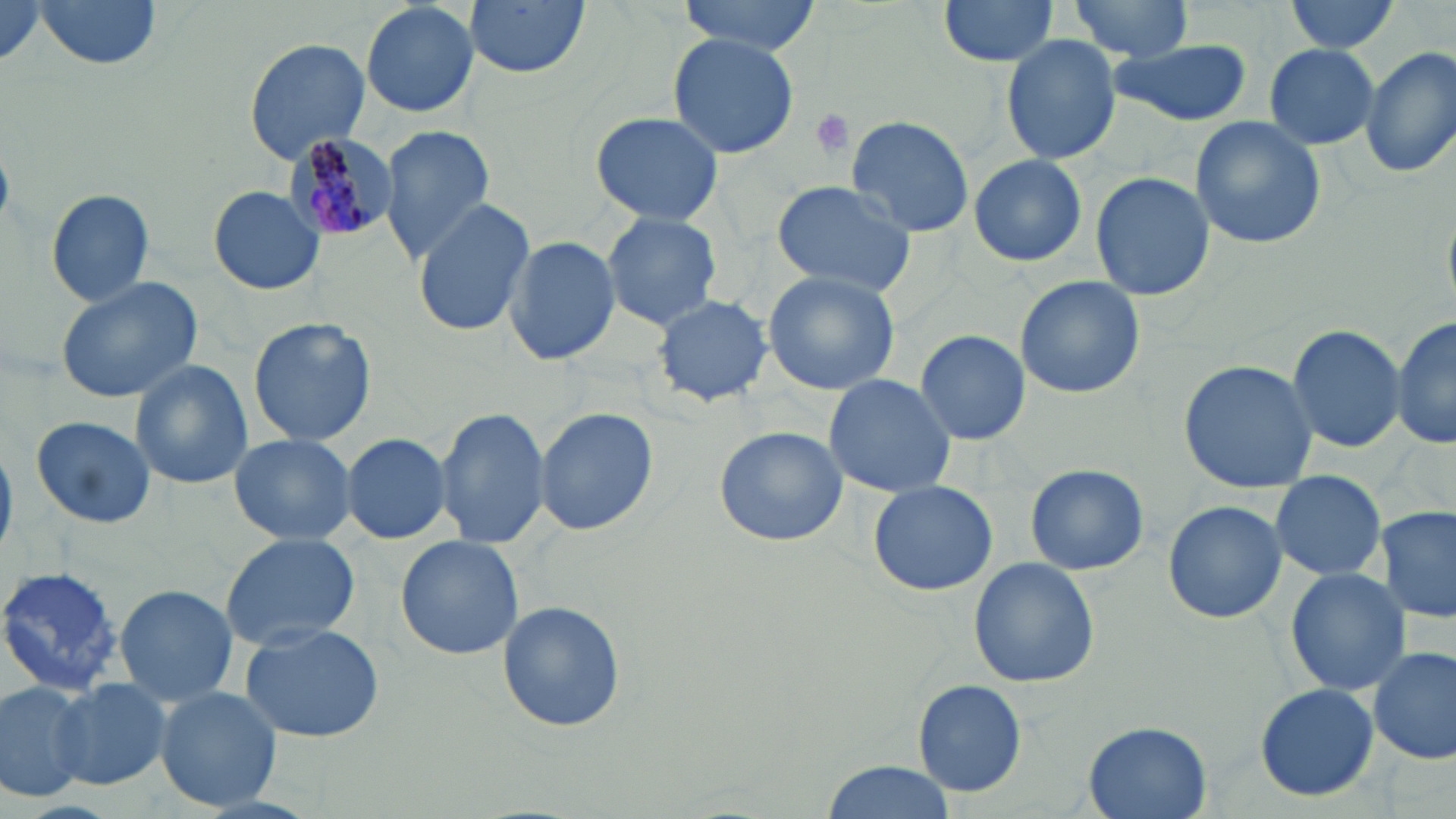
Summary:
  - Coordinate format: approximate bounding boxes as (x1,y1)-(x2,y2) corner pairs in pixels
  - Uninfected red blood cell locations: (35,0)-(165,70), (463,0)-(592,78), (675,0)-(823,55), (937,0)-(1061,69), (1063,0)-(1196,61), (1283,0)-(1403,54), (0,1)-(57,72), (360,2)-(481,118), (666,32)-(801,159), (1001,33)-(1123,167), (243,38)-(371,165), (1107,41)-(1252,126), (1262,42)-(1382,150), (1358,45)-(1456,178), (589,110)-(727,227), (846,114)-(975,239), (1189,116)-(1326,251), (380,125)-(497,263), (969,152)-(1089,268), (1089,170)-(1214,303), (770,180)-(918,297), (211,186)-(324,295), (45,189)-(155,308), (412,197)-(534,339), (601,211)-(726,332), (504,236)-(621,364), (761,268)-(901,396), (56,276)-(204,404), (1014,276)-(1146,397), (652,293)-(773,407), (1392,314)-(1454,452), (248,316)-(376,449), (1286,320)-(1408,455), (916,329)-(1031,446), (1177,358)-(1319,494), (130,359)-(254,490), (823,373)-(956,499), (436,404)-(550,550), (532,404)-(659,536), (29,415)-(155,532), (713,425)-(847,546), (341,432)-(451,544), (228,434)-(359,548), (1024,462)-(1150,575), (1268,470)-(1389,582), (867,480)-(998,597), (1163,498)-(1286,624), (1374,505)-(1455,625), (219,534)-(363,651), (395,535)-(525,661), (967,557)-(1100,688), (0,565)-(124,697), (1284,568)-(1413,696), (113,584)-(238,708), (496,600)-(626,731), (240,622)-(385,743), (1369,644)-(1455,767), (51,678)-(174,790), (914,680)-(1027,797), (0,681)-(91,804), (1253,682)-(1380,803), (155,686)-(285,812), (1083,722)-(1213,819), (820,760)-(955,819)
  - Platelet locations: (803,109)-(858,162)
  - Plasmodium malariae-infected red blood cell locations: (279,134)-(394,242)
  - Slide-level diagnosis: Plasmodium malariae
  - Magnification: 1000x
  - Stain: May-Grünwald-Giemsa
  - Preparation: thin blood smear
  - Field of view: single
  - Image size: 1456×819 pixels
  - Modality: optical microscopy